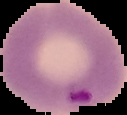

image size = 127×115 pixels
preparation = thin blood smear
malaria status = parasitized
image type = segmented cell region on a black background